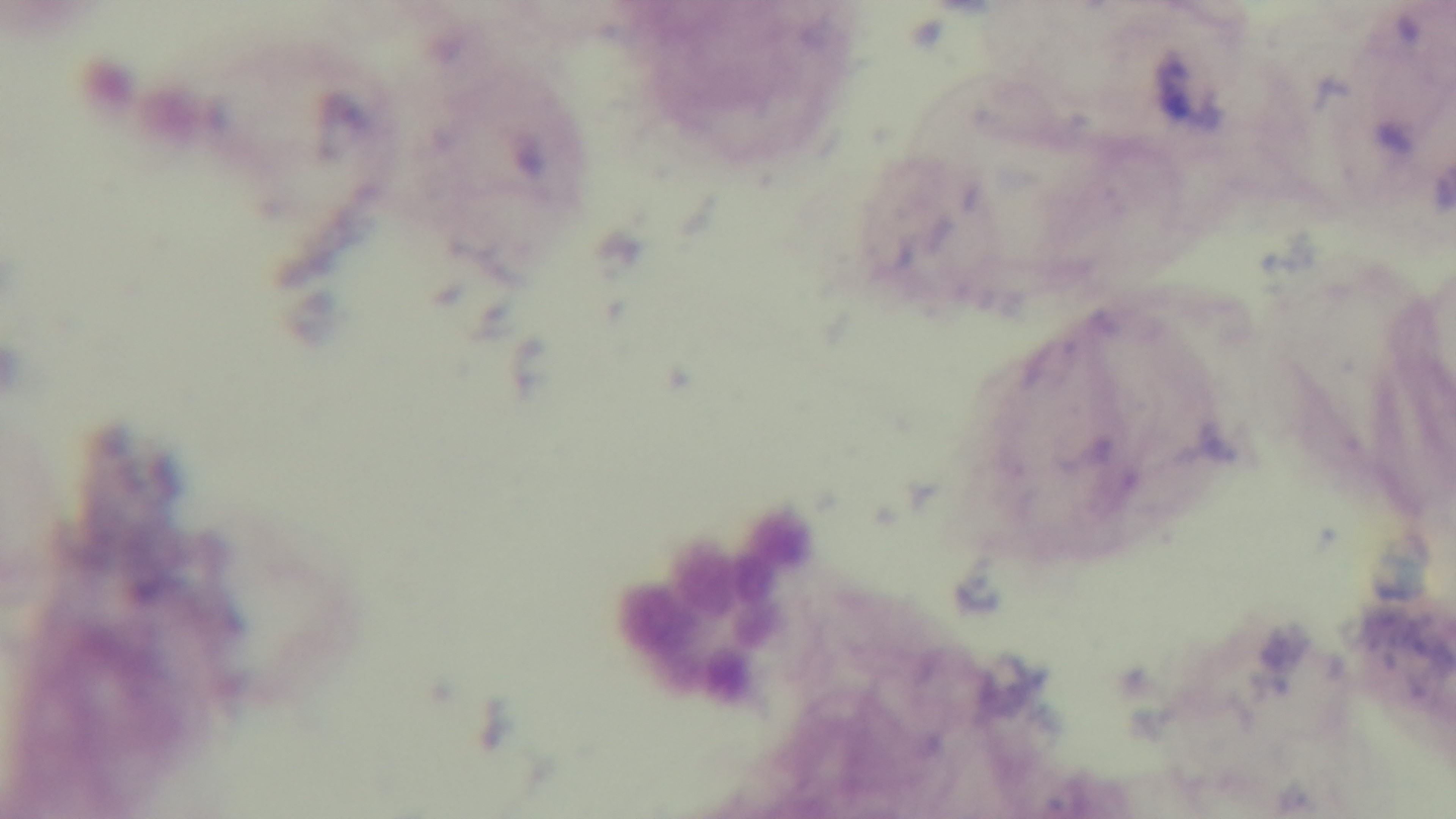
modality = light microscopy
objective = 100x oil immersion
preparation = thick
field of view = single
stain = Giemsa
capture = mounted 4K digital camera
malaria status = uninfected